Give the extent of all uninfected red blood cells.
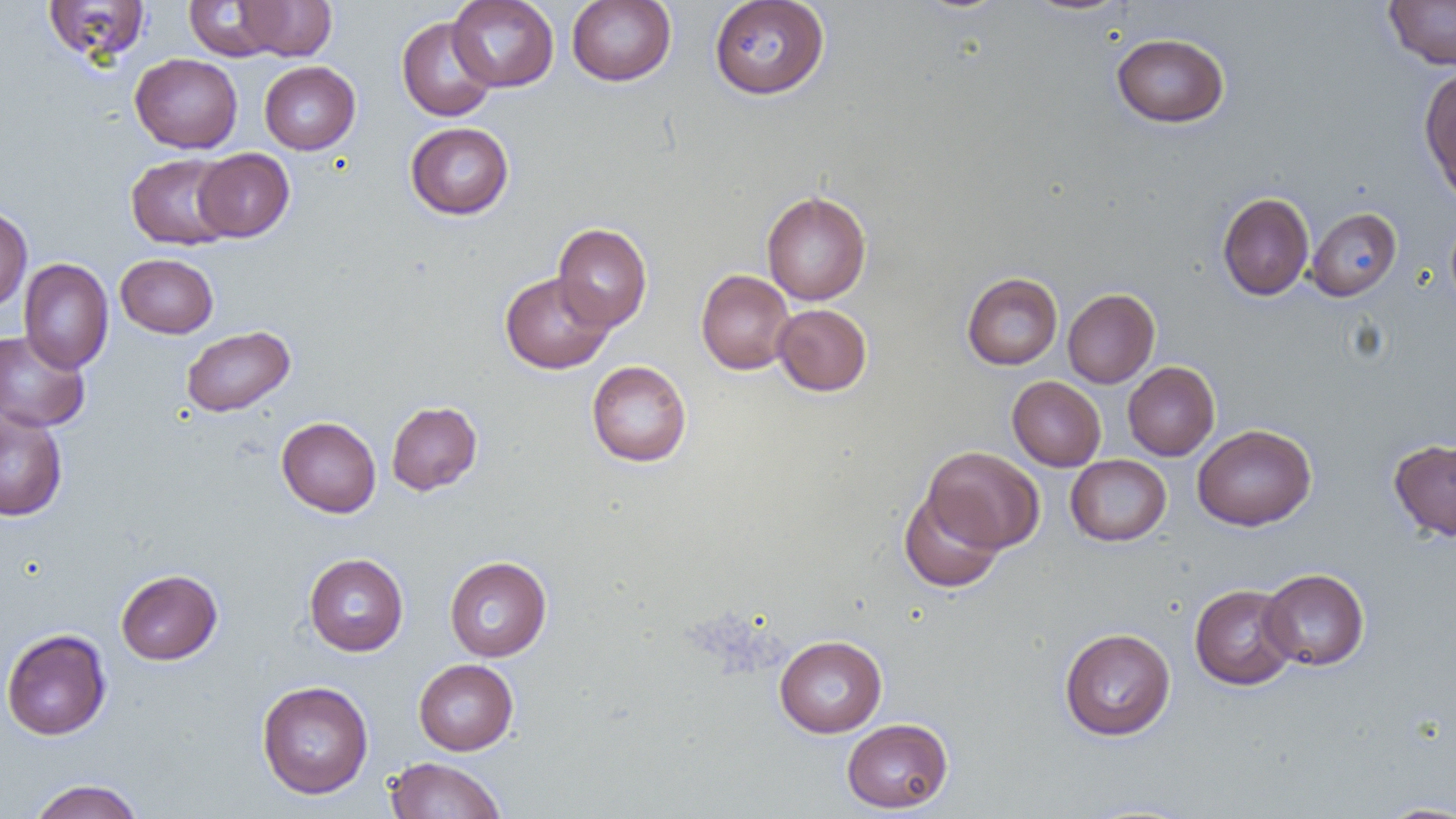
Approximate bounding boxes as named x1/y1/x2/y2 corners in pixels.
Uninfected red blood cells: (x1=43, y1=0, x2=150, y2=65), (x1=183, y1=0, x2=285, y2=60), (x1=447, y1=0, x2=559, y2=92), (x1=566, y1=0, x2=676, y2=86), (x1=708, y1=0, x2=830, y2=100), (x1=1021, y1=0, x2=1134, y2=16), (x1=235, y1=1, x2=336, y2=61), (x1=1384, y1=1, x2=1456, y2=69), (x1=396, y1=16, x2=498, y2=122), (x1=1112, y1=33, x2=1230, y2=128), (x1=130, y1=53, x2=243, y2=154), (x1=259, y1=61, x2=360, y2=154), (x1=1419, y1=65, x2=1456, y2=199), (x1=405, y1=122, x2=514, y2=219), (x1=193, y1=149, x2=294, y2=242), (x1=126, y1=153, x2=237, y2=249), (x1=761, y1=191, x2=871, y2=306), (x1=1217, y1=192, x2=1314, y2=301), (x1=0, y1=205, x2=32, y2=312), (x1=1305, y1=207, x2=1402, y2=301), (x1=552, y1=223, x2=652, y2=331), (x1=115, y1=253, x2=218, y2=338), (x1=18, y1=259, x2=114, y2=373), (x1=696, y1=269, x2=795, y2=374), (x1=499, y1=271, x2=615, y2=374), (x1=961, y1=272, x2=1063, y2=370), (x1=1062, y1=288, x2=1159, y2=387), (x1=773, y1=304, x2=872, y2=396), (x1=181, y1=325, x2=295, y2=417), (x1=0, y1=329, x2=91, y2=432), (x1=586, y1=360, x2=692, y2=467), (x1=1123, y1=362, x2=1219, y2=460), (x1=1007, y1=376, x2=1106, y2=471), (x1=386, y1=401, x2=482, y2=495), (x1=0, y1=407, x2=68, y2=521), (x1=276, y1=416, x2=381, y2=517), (x1=1192, y1=424, x2=1316, y2=531), (x1=1388, y1=437, x2=1456, y2=541), (x1=924, y1=446, x2=1045, y2=553), (x1=1065, y1=454, x2=1171, y2=546), (x1=898, y1=488, x2=1006, y2=592), (x1=304, y1=553, x2=408, y2=656), (x1=444, y1=556, x2=552, y2=661), (x1=1259, y1=568, x2=1370, y2=671), (x1=116, y1=569, x2=222, y2=664), (x1=1190, y1=584, x2=1299, y2=690), (x1=1059, y1=627, x2=1175, y2=740), (x1=1, y1=628, x2=112, y2=740), (x1=774, y1=635, x2=887, y2=737), (x1=414, y1=659, x2=518, y2=755), (x1=256, y1=680, x2=373, y2=799), (x1=841, y1=718, x2=953, y2=813), (x1=386, y1=756, x2=506, y2=819), (x1=27, y1=779, x2=146, y2=819), (x1=1375, y1=801, x2=1456, y2=818).

slide-level diagnosis = negative for blood parasites
preparation = thin blood film
modality = light microscopy
image size = 1456×819 pixels
magnification = 1000x
field of view = one of a larger specimen